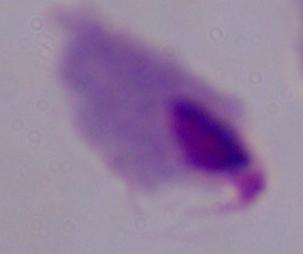
Summary:
  - Magnification: 1000x
  - Identification: trichomonad
  - Modality: photomicrograph